Name the blood parasite species.
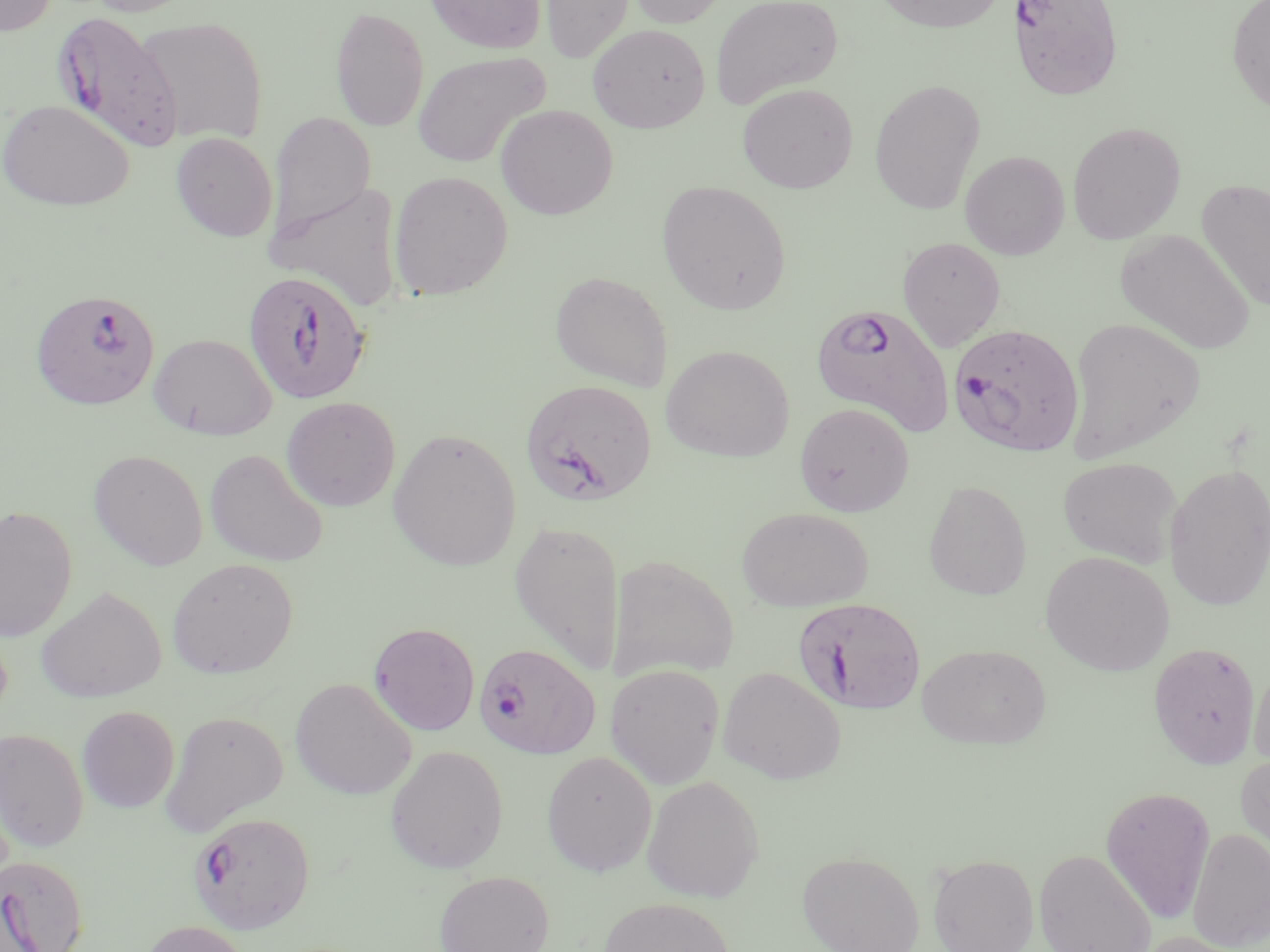

Plasmodium falciparum.

Approximate bounding boxes as named x1/y1/x2/y2 corners in pixels. Uninfected red blood cell locations: (x1=0, y1=0, x2=57, y2=36), (x1=83, y1=0, x2=198, y2=16), (x1=424, y1=0, x2=546, y2=54), (x1=540, y1=0, x2=634, y2=63), (x1=625, y1=0, x2=730, y2=28), (x1=711, y1=0, x2=843, y2=109), (x1=871, y1=0, x2=1008, y2=34), (x1=1226, y1=0, x2=1270, y2=115), (x1=330, y1=5, x2=429, y2=132), (x1=134, y1=16, x2=268, y2=145), (x1=587, y1=23, x2=710, y2=133), (x1=413, y1=51, x2=551, y2=167), (x1=869, y1=78, x2=986, y2=215), (x1=737, y1=83, x2=858, y2=193), (x1=0, y1=99, x2=134, y2=211), (x1=495, y1=104, x2=618, y2=220), (x1=268, y1=111, x2=376, y2=239), (x1=1067, y1=122, x2=1186, y2=245), (x1=171, y1=132, x2=278, y2=242), (x1=960, y1=150, x2=1069, y2=259), (x1=388, y1=171, x2=512, y2=299), (x1=267, y1=178, x2=404, y2=312), (x1=1197, y1=179, x2=1269, y2=311), (x1=657, y1=180, x2=792, y2=315), (x1=1116, y1=228, x2=1255, y2=354), (x1=897, y1=236, x2=1006, y2=351), (x1=550, y1=270, x2=673, y2=391), (x1=1065, y1=317, x2=1205, y2=462), (x1=148, y1=333, x2=276, y2=440), (x1=661, y1=344, x2=794, y2=462), (x1=281, y1=396, x2=401, y2=511), (x1=794, y1=402, x2=914, y2=517), (x1=388, y1=428, x2=521, y2=572), (x1=88, y1=449, x2=208, y2=570), (x1=205, y1=449, x2=329, y2=567), (x1=1058, y1=457, x2=1181, y2=567), (x1=1164, y1=463, x2=1270, y2=610), (x1=923, y1=480, x2=1032, y2=600), (x1=0, y1=505, x2=78, y2=642), (x1=736, y1=506, x2=873, y2=611), (x1=509, y1=519, x2=627, y2=675), (x1=1040, y1=551, x2=1174, y2=676), (x1=607, y1=553, x2=739, y2=681), (x1=167, y1=558, x2=299, y2=679), (x1=35, y1=586, x2=167, y2=703), (x1=369, y1=622, x2=480, y2=736), (x1=1148, y1=642, x2=1261, y2=769), (x1=918, y1=643, x2=1052, y2=749), (x1=1250, y1=655, x2=1270, y2=771), (x1=605, y1=663, x2=724, y2=789), (x1=717, y1=666, x2=847, y2=784), (x1=290, y1=677, x2=417, y2=800), (x1=77, y1=706, x2=179, y2=813), (x1=160, y1=710, x2=288, y2=836), (x1=0, y1=727, x2=89, y2=852), (x1=385, y1=744, x2=507, y2=874), (x1=541, y1=750, x2=658, y2=875), (x1=1235, y1=752, x2=1270, y2=870), (x1=641, y1=775, x2=765, y2=902), (x1=1100, y1=786, x2=1216, y2=924), (x1=1187, y1=828, x2=1270, y2=951), (x1=1033, y1=848, x2=1157, y2=952), (x1=796, y1=851, x2=925, y2=952), (x1=928, y1=853, x2=1039, y2=952), (x1=434, y1=870, x2=554, y2=952), (x1=598, y1=897, x2=736, y2=952), (x1=137, y1=919, x2=253, y2=952), (x1=1134, y1=931, x2=1256, y2=952). Plasmodium falciparum-infected red blood cell locations: (x1=1008, y1=0, x2=1123, y2=101), (x1=52, y1=12, x2=184, y2=152), (x1=242, y1=269, x2=372, y2=404), (x1=29, y1=288, x2=160, y2=411), (x1=811, y1=302, x2=955, y2=437), (x1=948, y1=323, x2=1085, y2=458), (x1=520, y1=379, x2=657, y2=506), (x1=793, y1=597, x2=926, y2=716), (x1=474, y1=644, x2=601, y2=759), (x1=188, y1=812, x2=315, y2=934), (x1=0, y1=854, x2=89, y2=952). One field of a larger specimen. May-Grünwald-Giemsa stain. Light microscopy. Image is 1270×952 pixels. Captured at 1000x magnification. Thin blood smear.